Identify the blood parasite species.
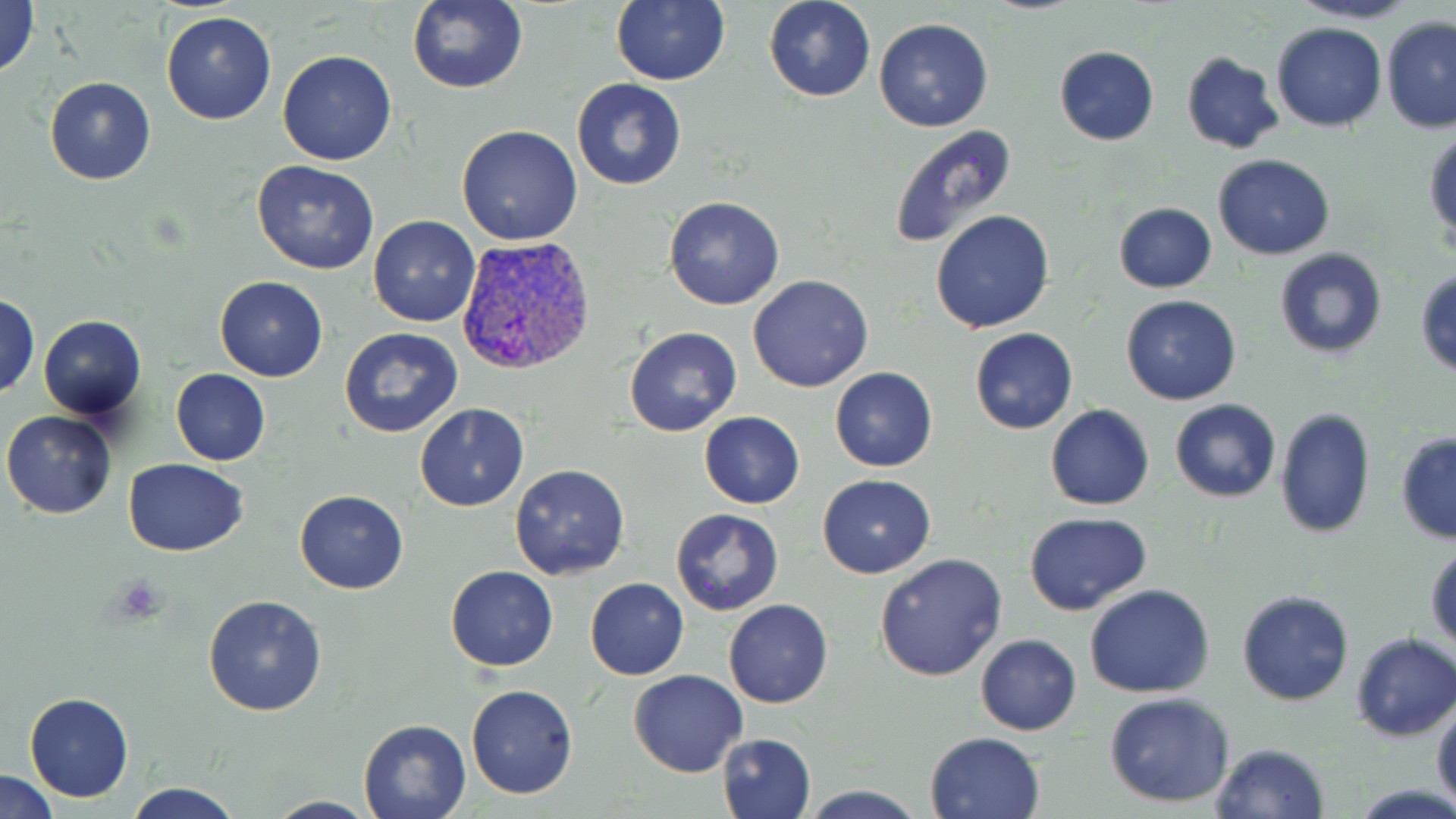

Plasmodium vivax.

Approximate bounding boxes as (x1,y1)-(x2,y2) corner pairs in pixels. Platelet locations: (110,577)-(169,622). Plasmodium vivax-infected red blood cell locations: (456,236)-(596,377). Uninfected red blood cell locations: (407,0)-(529,95), (763,0)-(876,102), (1288,0)-(1426,24), (0,1)-(40,81), (610,1)-(731,86), (162,11)-(276,124), (1380,16)-(1456,133), (873,18)-(994,132), (1269,22)-(1387,132), (1054,48)-(1160,145), (277,49)-(397,166), (1181,52)-(1285,155), (43,76)-(158,186), (571,78)-(686,190), (456,125)-(583,246), (888,125)-(1020,252), (1424,131)-(1455,250), (1212,153)-(1335,260), (252,160)-(380,275), (662,195)-(785,312), (1113,201)-(1216,293), (930,210)-(1056,333), (368,214)-(480,326), (1274,248)-(1388,359), (1415,268)-(1456,378), (747,274)-(874,392), (214,276)-(328,382), (1,294)-(39,398), (1120,294)-(1242,405), (37,315)-(148,419), (624,325)-(744,438), (969,327)-(1077,434), (338,328)-(464,440), (829,367)-(938,472), (172,368)-(270,465), (1170,399)-(1281,503), (414,403)-(529,512), (1046,404)-(1154,511), (1274,408)-(1375,540), (1,411)-(117,521), (698,411)-(804,509), (1395,433)-(1456,544), (123,458)-(250,558), (510,464)-(630,582), (817,474)-(936,578), (295,490)-(408,594), (670,508)-(784,616), (1023,511)-(1153,616), (1425,542)-(1456,652), (874,552)-(1008,682), (444,565)-(558,671), (585,577)-(689,679), (1085,584)-(1215,698), (1236,589)-(1355,706), (203,595)-(326,716), (724,599)-(834,708), (1350,632)-(1456,741), (976,633)-(1081,735), (628,670)-(748,777), (465,684)-(579,799), (24,693)-(132,802), (1104,693)-(1236,808), (1432,694)-(1456,808), (358,718)-(470,818), (925,730)-(1046,819), (717,732)-(815,819), (1210,742)-(1332,819), (0,771)-(59,818), (124,780)-(243,818), (799,784)-(924,818), (264,796)-(379,818). Thin blood smear. Optical microscopy. Image is 1456×819 pixels. Captured at 1000x magnification. May-Grünwald-Giemsa-stained preparation. One field of a larger specimen.